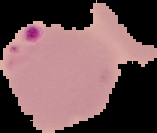
image size = 157×133 pixels
image type = segmented cell region on a black background
result = malaria parasites detected
preparation = thin blood smear